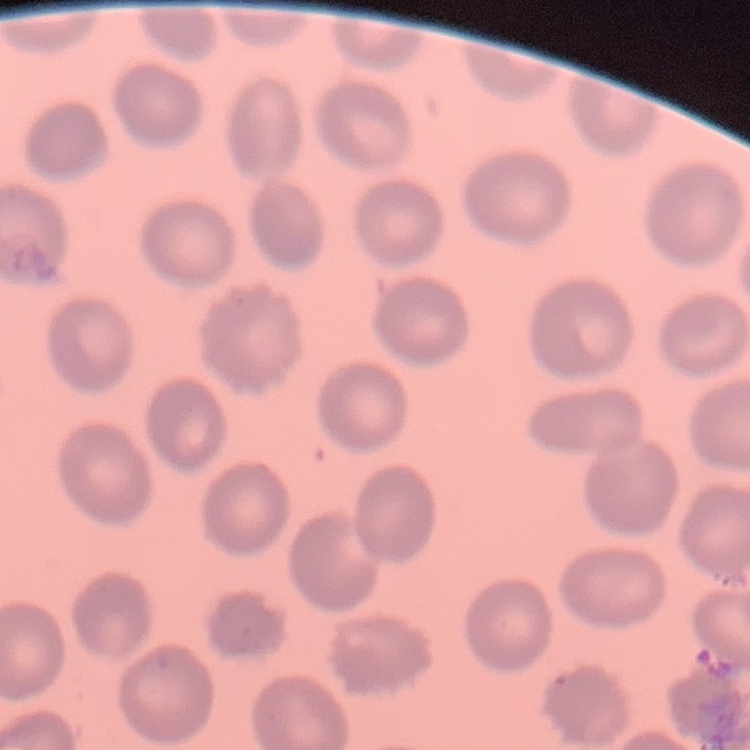
The red blood cells exhibit no rouleaux formation. Thin blood smear. Square crop of a larger photomicrograph. Field's or Giemsa stain.